Locate every blood parasite and identify its species.
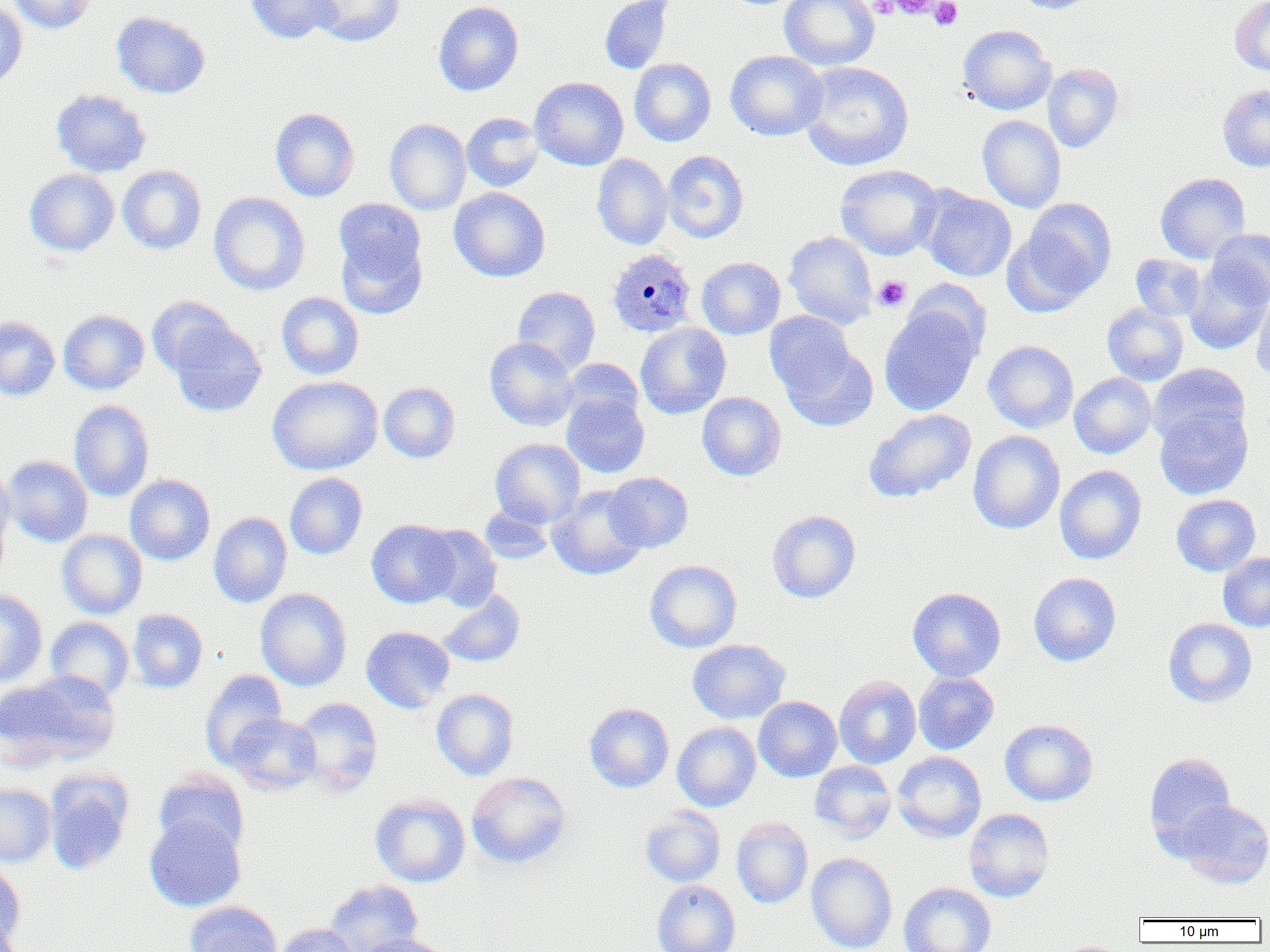

Approximate bounding boxes as (x1,y1)-(x2,y2) corner pairs in pixels.
Plasmodium ovale-infected red blood cells: (607,248)-(696,337).
No Plasmodium falciparum, Plasmodium malariae, Plasmodium vivax, Babesia divergens, or Trypanosoma brucei observed.

Summary:
  - Uninfected red blood cell locations: (10,0)-(97,34), (246,0)-(340,44), (307,0)-(405,46), (599,0)-(675,74), (779,0)-(879,70), (1014,0)-(1097,13), (1230,0)-(1270,76), (433,1)-(524,96), (0,3)-(27,90), (112,11)-(210,99), (958,24)-(1056,115), (725,50)-(827,141), (629,58)-(716,146), (799,61)-(914,170), (1042,63)-(1124,152), (530,77)-(628,170), (1217,84)-(1270,171), (51,88)-(151,177), (270,108)-(359,202), (461,112)-(544,192), (977,115)-(1066,213), (385,119)-(471,214), (662,150)-(748,243), (592,153)-(673,250), (117,165)-(207,254), (835,165)-(942,261), (24,169)-(120,256), (1155,172)-(1251,263), (449,187)-(550,282), (919,188)-(1017,282), (208,192)-(310,295), (334,198)-(426,286), (1023,198)-(1117,296), (1206,228)-(1270,307), (784,231)-(877,329), (336,232)-(427,319), (1001,232)-(1095,317), (1130,254)-(1206,322), (697,257)-(785,339), (1185,263)-(1270,355), (904,278)-(992,361), (512,286)-(600,374), (1251,290)-(1270,380), (276,292)-(364,380), (146,296)-(236,377), (1102,303)-(1188,386), (879,305)-(983,416), (58,310)-(149,394), (764,311)-(857,398), (0,316)-(60,401), (169,320)-(266,416), (635,323)-(731,419), (485,337)-(579,431), (983,340)-(1078,433), (781,343)-(878,432), (560,358)-(644,428), (1148,363)-(1250,447), (1069,373)-(1156,458), (267,375)-(382,475), (379,382)-(460,463), (697,391)-(786,481), (561,392)-(649,478), (69,400)-(154,501), (1154,406)-(1253,500), (863,409)-(976,503), (967,430)-(1064,534), (490,438)-(586,527), (2,455)-(92,547), (1054,464)-(1147,565), (0,465)-(15,558), (284,472)-(367,560), (606,472)-(693,553), (125,475)-(215,565), (547,484)-(647,580), (1171,494)-(1261,576), (0,500)-(11,589), (480,504)-(554,564), (767,510)-(861,603), (209,512)-(292,608), (366,519)-(458,608), (418,524)-(502,611), (57,529)-(147,619), (1218,551)-(1270,631), (645,560)-(742,652), (1029,573)-(1121,666), (907,587)-(1006,681), (255,588)-(352,691), (0,589)-(47,687), (437,589)-(525,667), (128,609)-(207,693), (45,617)-(134,702), (1163,618)-(1257,708), (361,626)-(455,713), (687,639)-(790,724), (200,670)-(287,769), (1,671)-(121,768), (913,671)-(999,754), (834,675)-(921,769), (431,689)-(519,780), (754,696)-(841,782), (294,697)-(383,796), (584,703)-(674,792), (227,713)-(321,794), (1000,719)-(1098,806), (672,721)-(761,811), (892,751)-(986,843), (1144,752)-(1236,852), (809,760)-(897,842), (153,769)-(250,856), (467,771)-(571,868), (44,772)-(133,875), (0,783)-(55,866), (370,795)-(470,888), (1174,799)-(1270,888), (641,807)-(725,887), (964,808)-(1055,902), (144,814)-(246,912), (731,817)-(813,909), (806,852)-(897,952), (0,860)-(26,948), (324,880)-(422,952), (652,880)-(740,952), (899,882)-(996,952), (185,901)-(282,952), (274,923)-(362,952), (356,934)-(450,952), (1056,941)-(1127,952)
  - Platelet locations: (869,0)-(897,17), (889,0)-(937,19), (929,0)-(962,29), (873,275)-(911,311)
  - Slide-level diagnosis: Plasmodium ovale
  - Magnification: 1000x
  - Preparation: thin blood film
  - Modality: light microscopy
  - Field of view: single
  - Image size: 1270×952 pixels